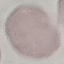

Result: negative for malaria parasites. Acquired by smartphone through the microscope eyepiece. Thin blood film. Automatically extracted cell patch, resized to 64 × 64 pixels. Giemsa stain.